Assess this cell for malaria.
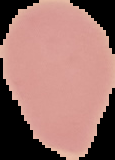

Uninfected.

Summary:
  - Image type: segmented cell region on a black background
  - Preparation: thin blood smear
  - Image size: 115×160 pixels